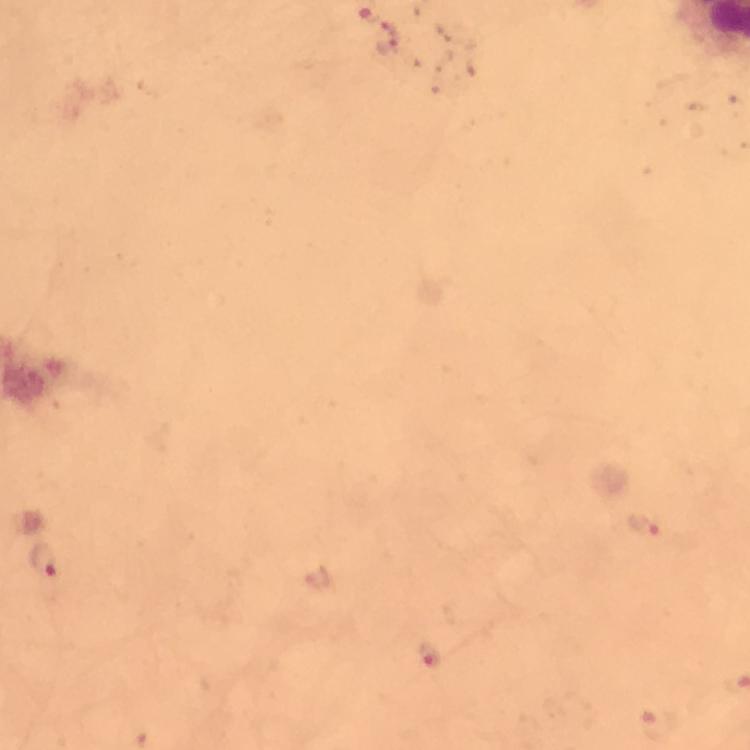
Approximate centers as [x, y] in pixels.
Summary:
  - Plasmodium parasite locations: [388, 39], [643, 525], [46, 561], [319, 580], [430, 656], [659, 725]
  - Image size: 750×750 pixels
  - Magnification: 100x
  - Capture: smartphone camera through the microscope
  - Cropped from: a single field of view
  - Preparation: thick blood smear
  - Context: from a malaria diagnostic workup
  - Immersion oil: used
  - Stain: Giemsa